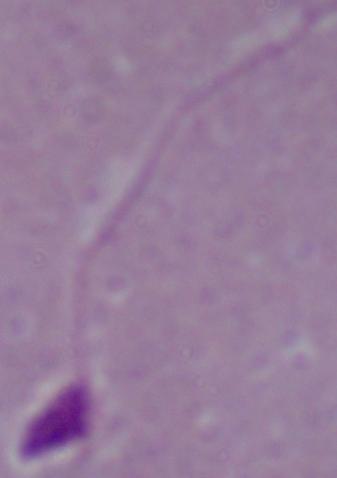
Summary:
  - Identification: Leishmania
  - Modality: photomicrograph
  - Magnification: 1000x